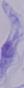
Summary:
  - Magnification: 1000x
  - Identification: trypanosome
  - Modality: photomicrograph